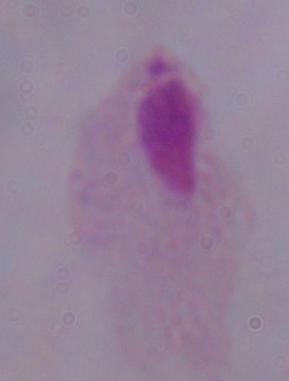 A trichomonad is shown. 1000x magnification. Micrograph.